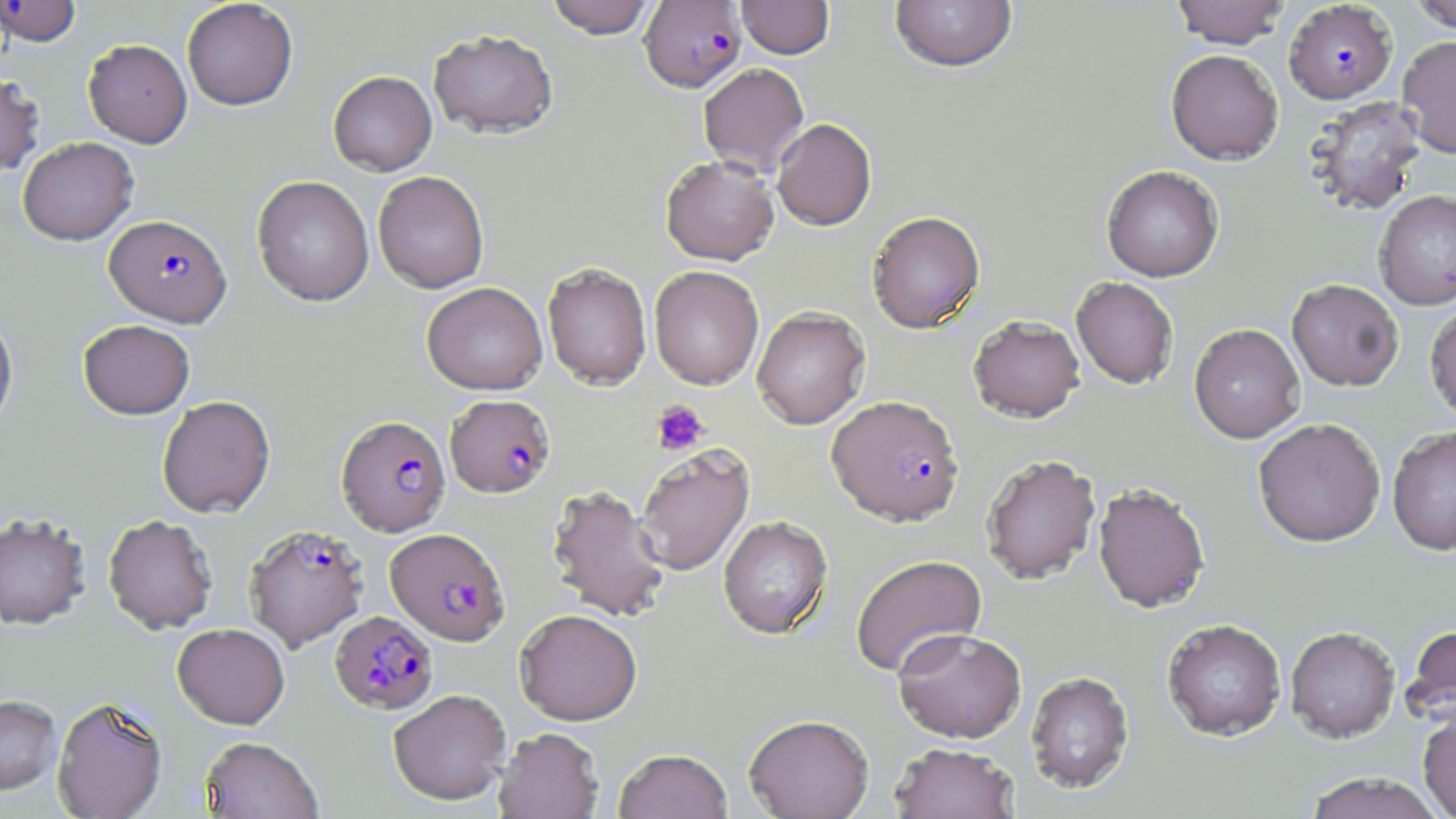
slide_level_diagnosis: Plasmodium falciparum
stain: May-Grünwald-Giemsa
modality: optical microscopy
plasmodium_falciparum_infected_red_blood_cell_locations: 'approximate bounding boxes as (x1, y1, x2, y2) in pixels: (1, 0, 84, 46), (639, 1, 746, 92), (1284, 1, 1397, 104), (104, 214, 232, 327), (445, 394, 555, 497), (826, 395, 965, 527), (336, 415, 450, 535), (244, 523, 368, 651), (385, 527, 510, 646), (330, 610, 438, 713)'
magnification: 1000x
preparation: thin blood film
image_size: 1456×819 pixels
platelet_locations: 'approximate bounding boxes as (x1, y1, x2, y2) in pixels: (652, 399, 709, 455)'
field_of_view: one of a larger specimen
uninfected_red_blood_cell_locations: 'approximate bounding boxes as (x1, y1, x2, y2) in pixels: (182, 0, 298, 110), (545, 0, 657, 38), (737, 0, 835, 59), (1170, 0, 1291, 48), (1409, 0, 1456, 32), (889, 1, 1017, 72), (429, 29, 559, 138), (1397, 35, 1456, 158), (83, 39, 193, 148), (1166, 49, 1283, 165), (698, 63, 809, 175), (0, 71, 45, 178), (328, 71, 437, 176), (1304, 95, 1426, 216), (772, 118, 877, 230), (17, 136, 139, 245), (661, 155, 778, 266), (1101, 165, 1224, 282), (373, 171, 489, 293), (252, 175, 374, 306), (1373, 190, 1456, 311), (866, 210, 985, 333), (542, 262, 652, 390), (649, 265, 764, 389), (1071, 276, 1179, 389), (1287, 279, 1403, 391), (422, 282, 548, 395), (1425, 302, 1456, 423), (752, 306, 870, 429), (0, 309, 18, 435), (968, 314, 1085, 422), (78, 319, 195, 419), (1189, 323, 1305, 443), (157, 395, 275, 518), (1253, 418, 1386, 548), (1387, 426, 1456, 556), (635, 445, 755, 576), (981, 454, 1101, 585), (1093, 483, 1211, 614), (546, 484, 670, 623), (0, 512, 92, 630), (103, 514, 218, 633), (718, 516, 833, 638), (850, 554, 987, 678), (514, 609, 643, 726), (1162, 619, 1286, 742), (172, 623, 290, 729), (1402, 623, 1456, 730), (892, 627, 1027, 743), (1285, 627, 1401, 744), (1026, 671, 1134, 794), (388, 688, 511, 806), (0, 695, 62, 794), (51, 696, 167, 819), (1418, 709, 1456, 818), (743, 714, 875, 818), (493, 727, 604, 818), (199, 736, 323, 818), (889, 743, 1020, 819), (613, 748, 733, 819), (1302, 772, 1447, 819)'